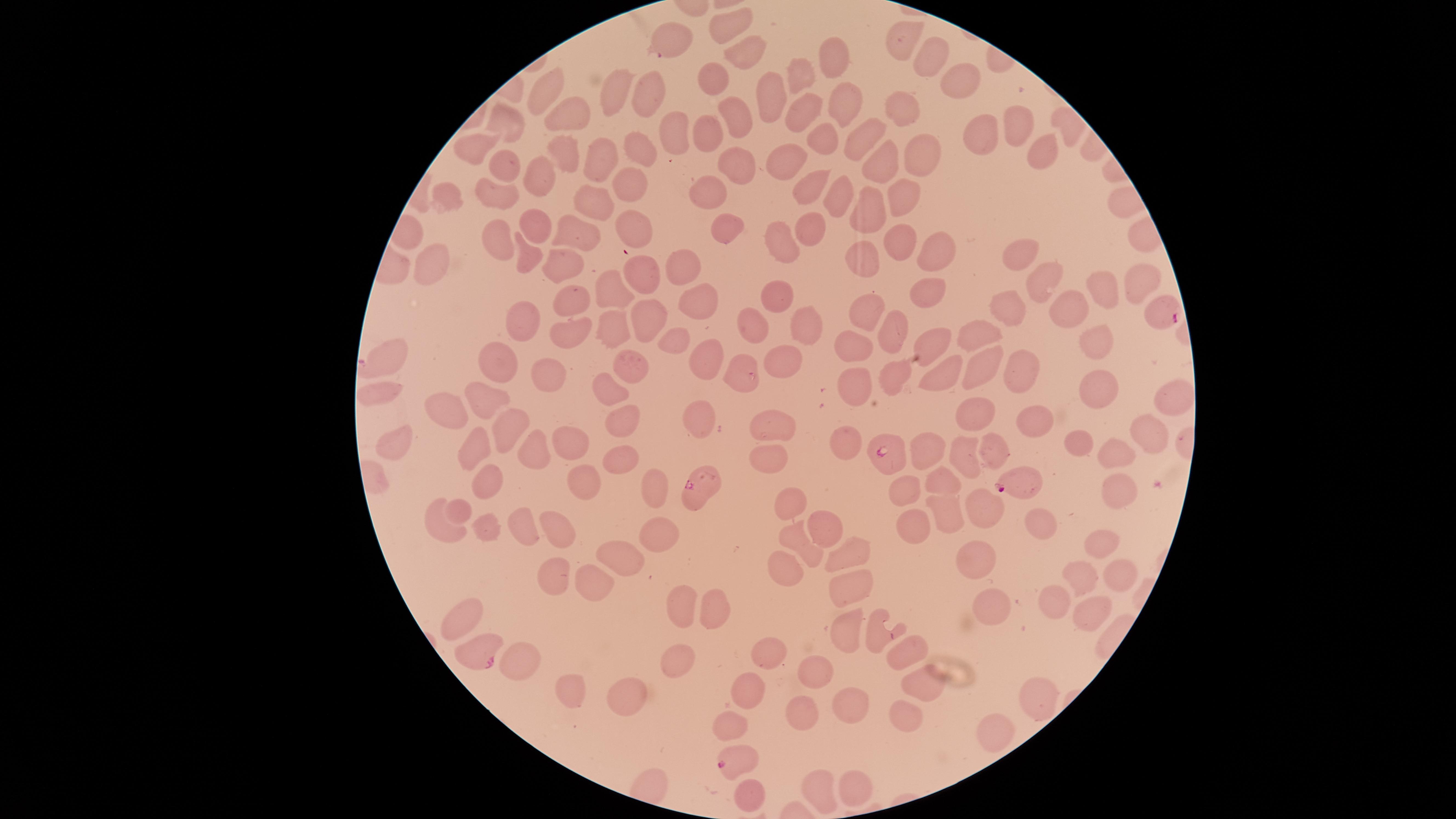 Approximate marker points as (x, y) in pixels. Uninfected red blood cells: (727, 26), (902, 38), (670, 40), (748, 60), (930, 62), (825, 64), (805, 76), (711, 78), (959, 81), (650, 90), (545, 92), (610, 93), (769, 97), (841, 105), (897, 109), (734, 114), (565, 118), (806, 118), (1016, 120), (508, 122), (676, 132), (705, 132), (865, 134), (983, 135), (821, 140), (479, 144), (1036, 150), (564, 153), (913, 154), (642, 155), (596, 157), (786, 159), (878, 163), (731, 164), (501, 171), (536, 179), (810, 183), (628, 185), (839, 192), (712, 195), (445, 196), (493, 196), (899, 196), (589, 197), (870, 204), (633, 223), (537, 226), (807, 227), (730, 232), (572, 234), (501, 235), (783, 241), (898, 244), (937, 254), (1018, 256), (863, 259), (528, 260), (425, 266), (556, 266), (684, 266), (639, 277), (1047, 282), (1138, 285), (931, 288), (1104, 289), (608, 292), (778, 302), (572, 306), (699, 306), (1075, 306), (1005, 309), (864, 312), (645, 316), (804, 324), (754, 325), (520, 326), (892, 329), (608, 330), (1096, 336), (935, 337), (568, 338), (674, 339), (975, 339), (851, 348), (390, 357), (630, 361), (704, 361), (783, 363), (498, 364), (983, 364), (944, 368), (1020, 368), (747, 369), (548, 377), (893, 377), (856, 386), (1095, 389), (1174, 390), (613, 392), (385, 395), (488, 403), (980, 413), (452, 415), (1040, 420), (622, 421), (699, 423), (771, 424), (1147, 424), (509, 426), (565, 436), (399, 442), (846, 442), (1084, 442), (931, 446), (764, 447), (478, 449), (1115, 451), (997, 452), (964, 453), (625, 458), (538, 460), (581, 470), (484, 483), (942, 484), (905, 485), (1114, 485), (653, 487), (790, 498), (459, 510), (982, 510), (949, 513), (817, 524), (484, 525), (438, 528), (522, 528), (1037, 529), (913, 530), (565, 534), (666, 537), (801, 541), (1096, 543), (850, 551), (984, 551), (626, 555), (782, 568), (554, 571), (1084, 576), (597, 579), (1117, 581), (846, 590), (680, 605), (1059, 605), (707, 609), (1090, 611), (468, 612), (982, 613), (846, 628), (881, 636), (904, 650), (771, 652), (520, 661), (681, 662), (818, 673), (748, 686), (921, 687), (573, 694), (1031, 694), (630, 698), (845, 699), (803, 705), (907, 713), (733, 718), (993, 730), (852, 776), (815, 785), (748, 794). Parasitized red blood cells: (1162, 313), (890, 458), (702, 486), (1022, 486), (482, 650), (738, 760). Thin blood film. Photographed with a smartphone camera through the microscope eyepiece. Giemsa-stained preparation. Species: Plasmodium falciparum. Presence: malaria parasites detected. Circular visible region. One field of view of the specimen. Image is 1456×819 pixels.